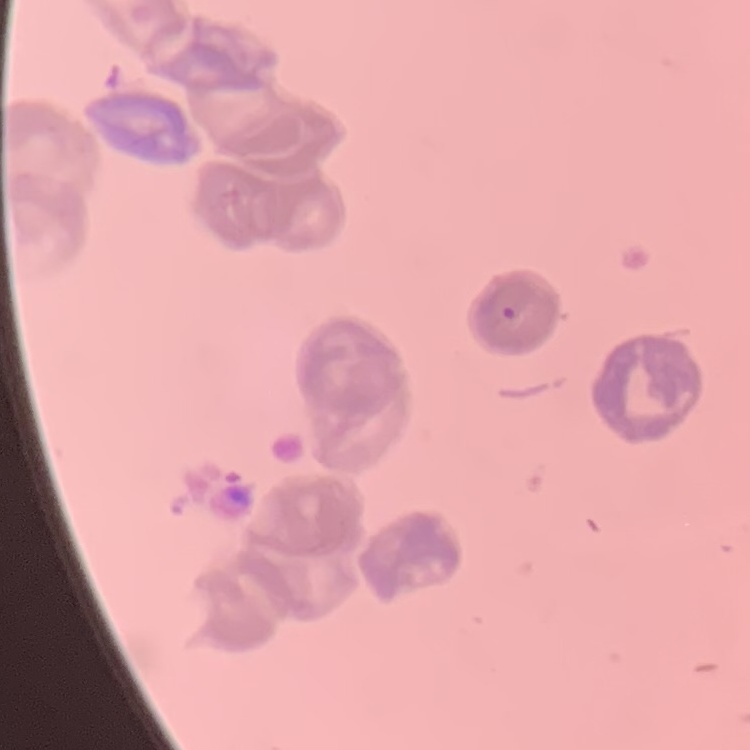
Summary:
  - Red blood cell morphology: rouleaux formation
  - Stain: Field's or Giemsa
  - Preparation: thin blood film
  - Image type: square crop of a larger photomicrograph